Point out malaria parasites and leukocytes.
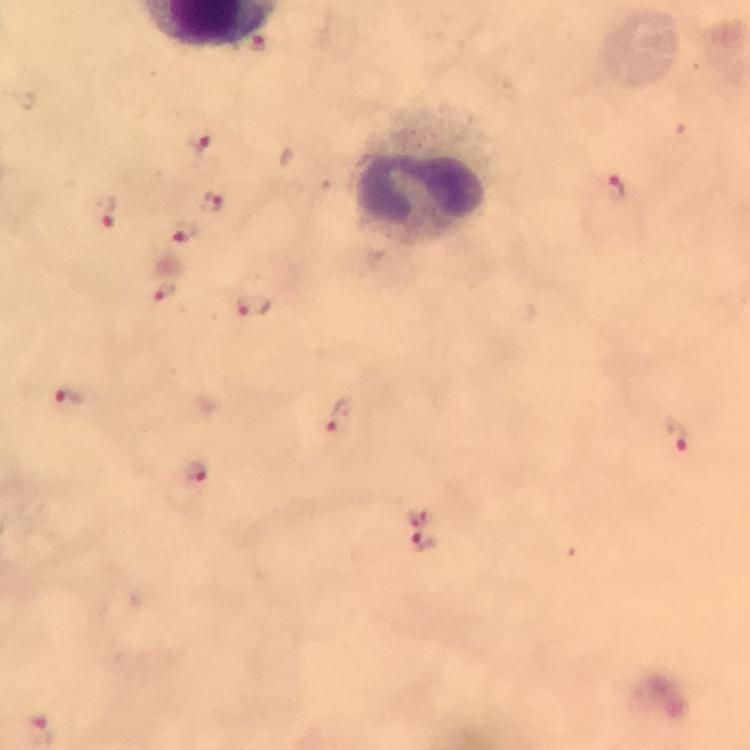
Approximate centers as [x, y] in pixels.
Malaria parasites: [254, 46], [201, 142], [613, 187], [211, 203], [105, 211], [186, 232], [164, 292], [254, 304], [69, 399], [336, 417], [678, 434], [196, 472], [419, 516], [422, 542], [40, 729].
Leukocytes: [425, 172].

Giemsa-stained preparation. From a diagnostic examination for malaria. Image is 750×750 pixels. Cropped region of a single field of view. Immersion oil applied. At 100x magnification. Thick blood film. Photographed with a smartphone mounted on the microscope.